Identify the parasite.
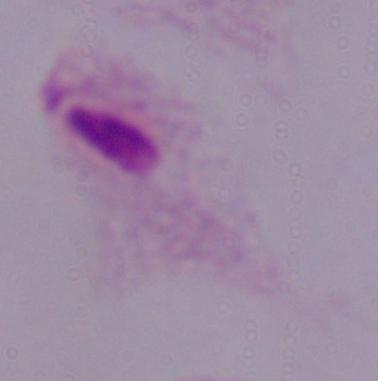

This is a trichomonad.

Summary:
  - Modality: photomicrograph
  - Magnification: 1000x